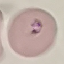

Summary:
  - Result: malaria parasites identified
  - Capture: smartphone through the microscope eyepiece
  - Stain: Giemsa
  - Image type: automatically extracted cell patch, resized to 64 × 64 pixels
  - Preparation: thin blood film